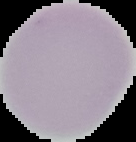

preparation: thin blood smear
result: no Plasmodium parasites detected
image_type: cell region segmented out of the field of view; surrounding area masked to black
image_size: 136×142 pixels